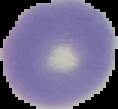
Summary:
  - Preparation: thin blood smear
  - Image type: segmented cell region with the area outside set to black
  - Image size: 118×109 pixels
  - Malaria status: uninfected